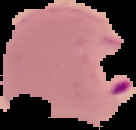 The area outside the segmented cell region is set to black. Image is 136×130 pixels. Result: Plasmodium parasites detected. From a thin blood smear.